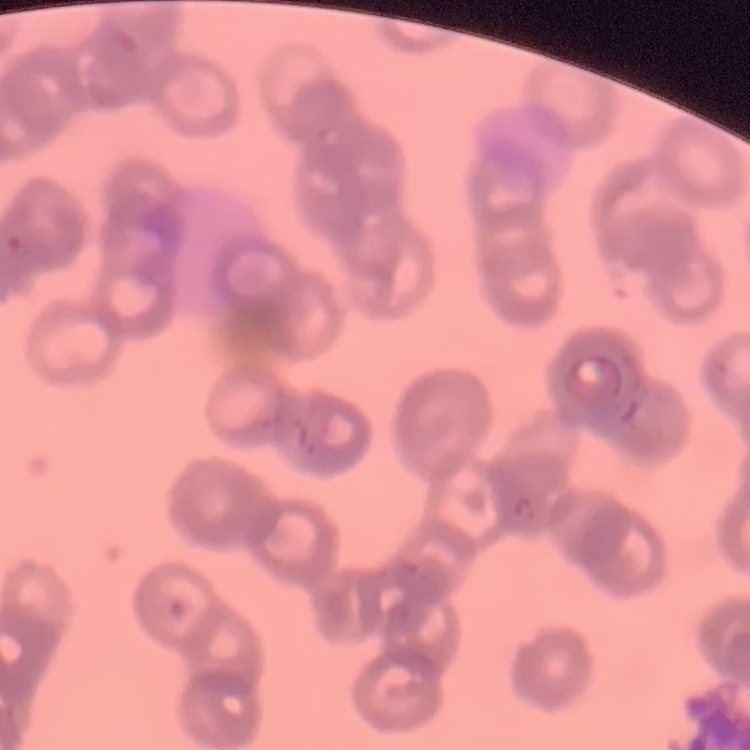
The red blood cells show rouleaux formation. One tile cut from a larger photomicrograph. Thin peripheral smear. Field's or Giemsa stain.